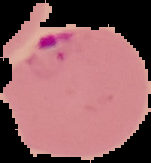
Summary:
  - Preparation: thin blood film
  - Image size: 151×163 pixels
  - Image type: segmented cell region on a black background
  - Malaria status: parasitized